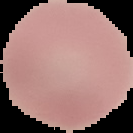

image type = segmented cell region on a black background
malaria status = uninfected
image size = 133×133 pixels
preparation = thin blood film